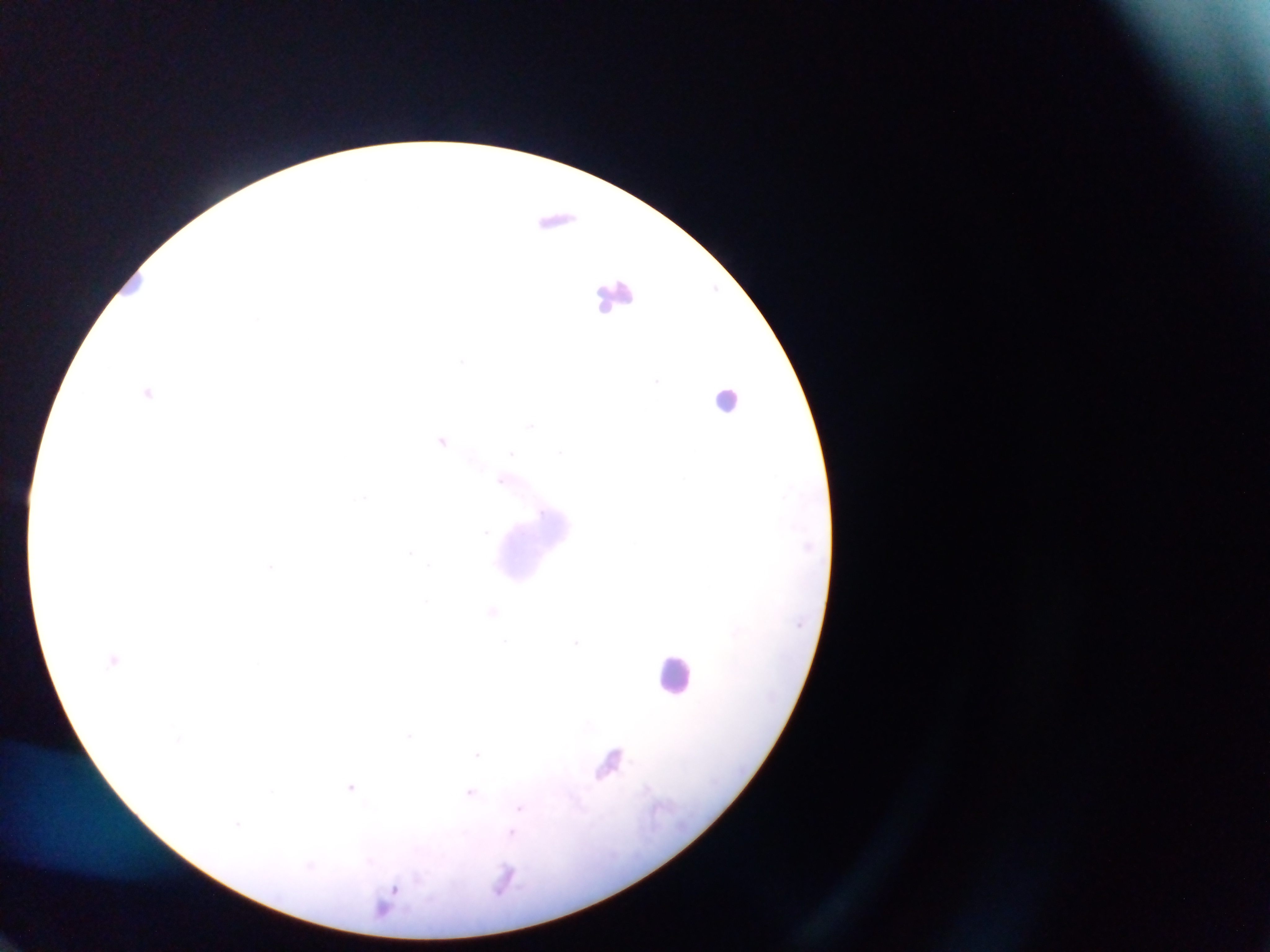
Approximate centers as x y in pixels. Plasmodium parasite locations: 556 217; 148 392; 442 439; 576 640; 614 759; 351 787; 647 788; 471 792; 393 889. Leukocyte locations: 609 303; 726 393; 675 678. Image is 1270×952 pixels. Mobile-phone photograph taken through the microscope. One field of view. Sample from Ghana. Thick blood smear.